Report the malaria status of this cell.
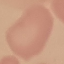

Uninfected.

preparation: thin blood film
stain: Giemsa
capture: smartphone through the microscope eyepiece
image_type: cell patch, automatically extracted from a larger field of view and resized to 64 × 64 pixels